Name the parasite shown.
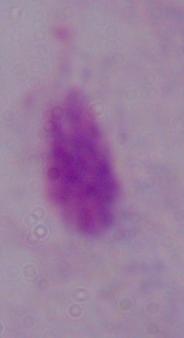

A trichomonad.

modality = micrograph
magnification = 1000x